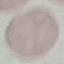

result = no malaria parasites detected
preparation = thin blood smear
stain = Giemsa
image type = automatically extracted cell patch, resized to 64 × 64 pixels
capture = smartphone through the microscope eyepiece